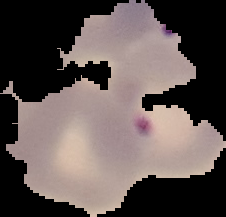

Summary:
  - Malaria status: parasitized
  - Image size: 226×217 pixels
  - Image type: segmented cell region with the area outside set to black
  - Preparation: thin blood smear